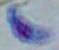

Summary:
  - Identification: Toxoplasma gondii
  - Magnification: 1000x
  - Modality: photomicrograph